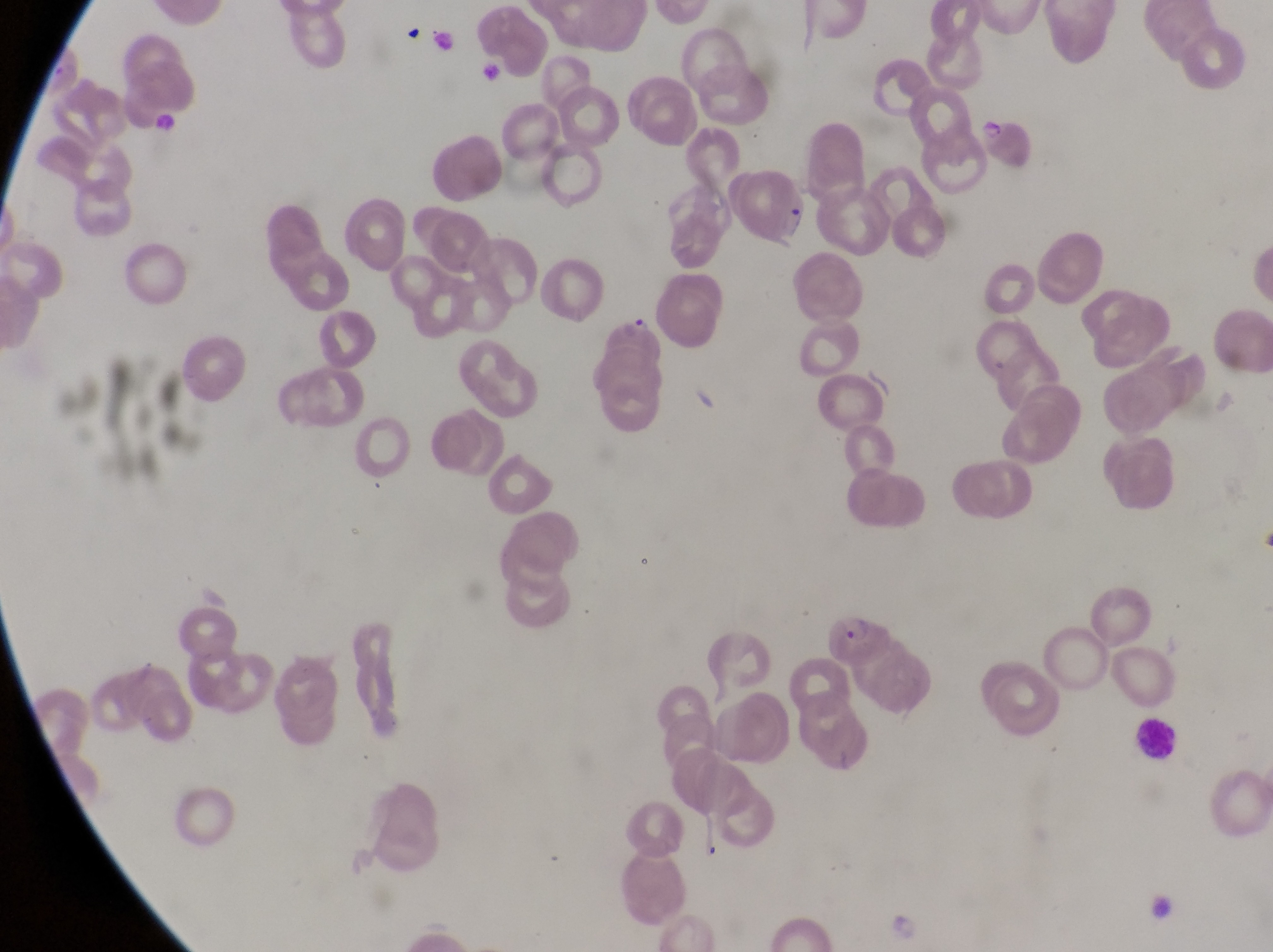
Approximate bounding boxes as left top right bottom in pixels. Parasitised red blood cell locations: 981 116 1037 168; 741 162 813 250; 601 300 668 377; 819 610 888 668. Artifact (platelet-like body, stain precipitate, or debris) locations: 401 24 435 50; 1151 899 1178 926. Leukocyte locations: 1138 711 1186 767. Thin blood film. Captured by a smartphone held over the eyepiece of an Olympus CX-23 microscope. Image is 1273×952 pixels. Collected in Uganda. One field of view. Magnification of 1000x.